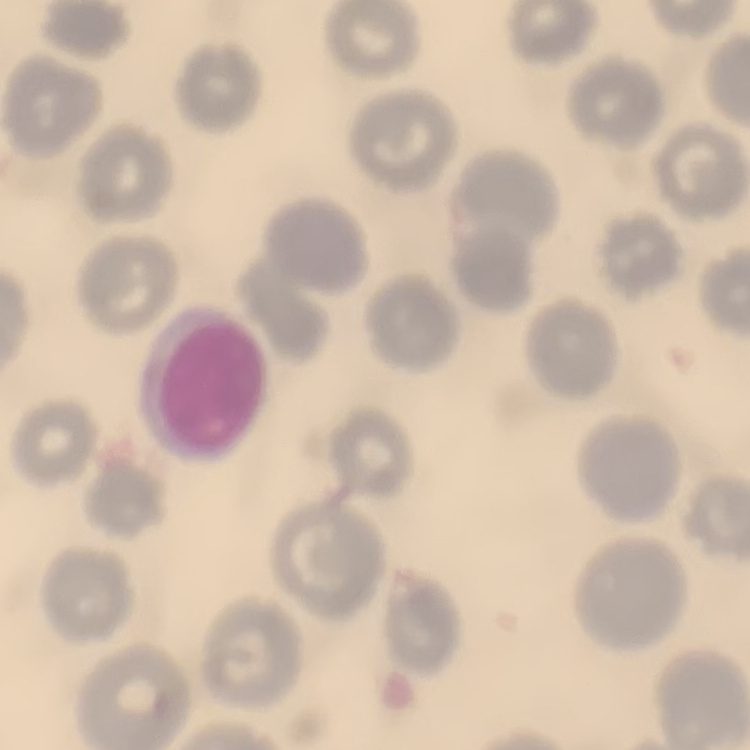 The red blood cells exhibit no rouleaux formation. Thin peripheral smear. Stained with either Field's or Giemsa. One tile cut from a larger photomicrograph.